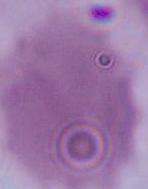
Summary:
  - Modality: micrograph
  - Magnification: 1000x
  - Identification: erythrocyte